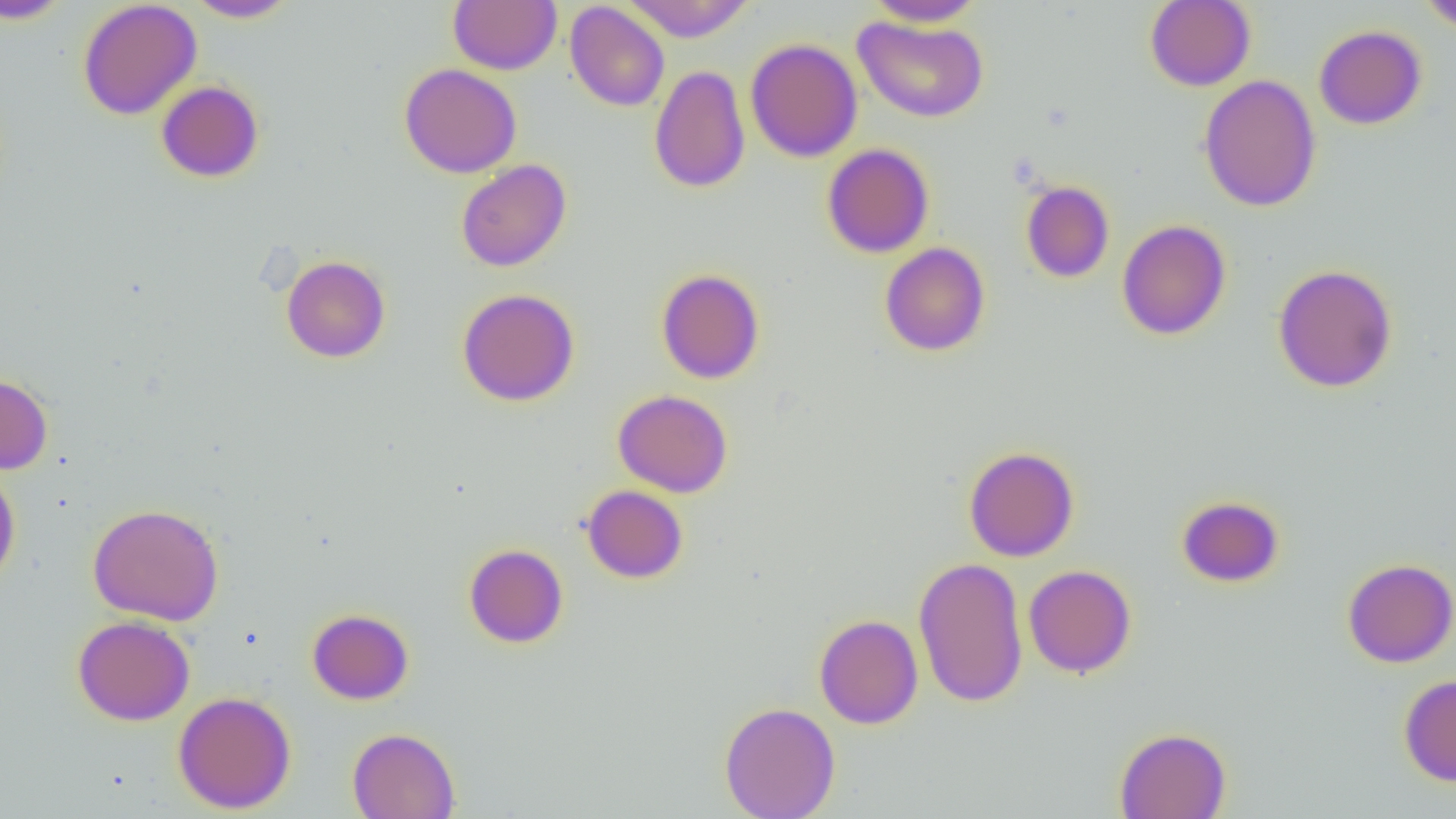

slide-level diagnosis = no evidence of blood parasites
magnification = 1000x
uninfected red blood cell locations = approximate bounding boxes as [x1, y1, x2, y2] in pixels: [0, 0, 73, 25], [185, 0, 299, 22], [621, 0, 756, 42], [864, 0, 986, 27], [1144, 0, 1256, 91], [1419, 0, 1456, 33], [77, 1, 202, 120], [449, 1, 562, 74], [565, 2, 669, 111], [852, 15, 989, 123], [1314, 25, 1427, 129], [745, 38, 862, 163], [398, 63, 521, 178], [649, 65, 751, 193], [1198, 75, 1322, 212], [156, 80, 265, 182], [822, 143, 935, 258], [456, 159, 572, 272], [1020, 180, 1115, 283], [1116, 219, 1231, 340], [879, 242, 990, 356], [281, 255, 391, 363], [1273, 263, 1398, 393], [656, 268, 765, 384], [457, 288, 580, 406], [0, 373, 53, 474], [613, 389, 733, 497], [963, 446, 1079, 562], [0, 465, 21, 591], [582, 485, 688, 583], [1176, 495, 1285, 588], [87, 503, 224, 626], [464, 543, 568, 648], [913, 556, 1029, 708], [1342, 558, 1456, 668], [1023, 564, 1137, 678], [307, 608, 414, 704], [814, 614, 923, 729], [72, 615, 195, 726], [1398, 674, 1456, 786], [173, 691, 296, 814], [719, 701, 840, 819], [347, 727, 461, 819], [1114, 727, 1231, 819]
field of view = single
modality = light microscopy
preparation = thin blood smear
image size = 1456×819 pixels